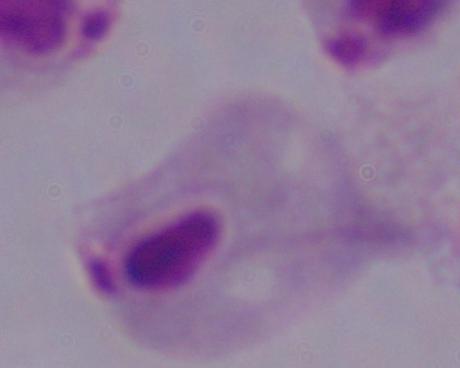

A trichomonad is shown. 1000x magnification. Photomicrograph.